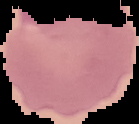

Summary:
  - Image type: segmented cell region with the area outside set to black
  - Result: malaria parasites detected
  - Preparation: thin blood smear
  - Image size: 139×124 pixels